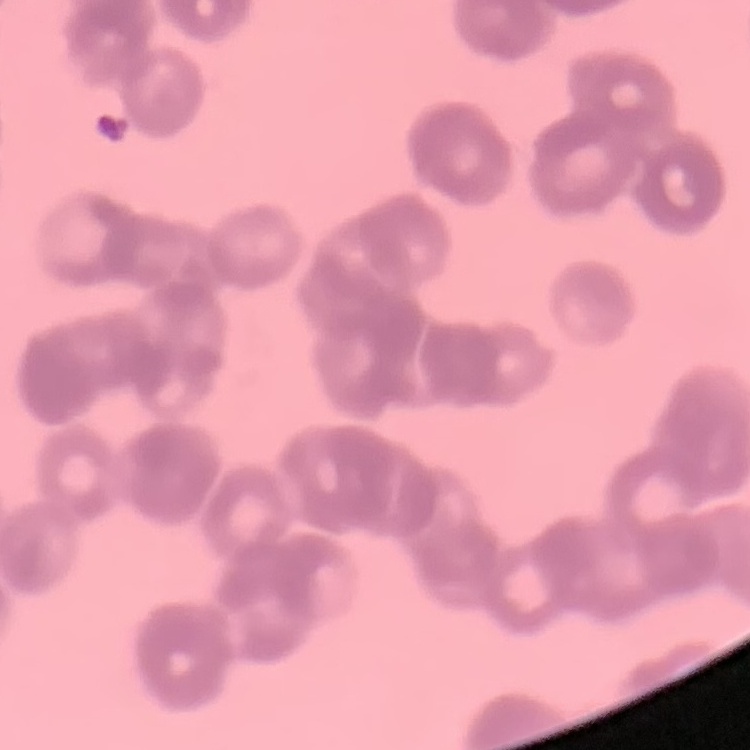
The red blood cells exhibit rouleaux formation. Square crop of a larger photomicrograph. Thin peripheral smear. Stained with either Field's or Giemsa.